Name the blood parasite species.
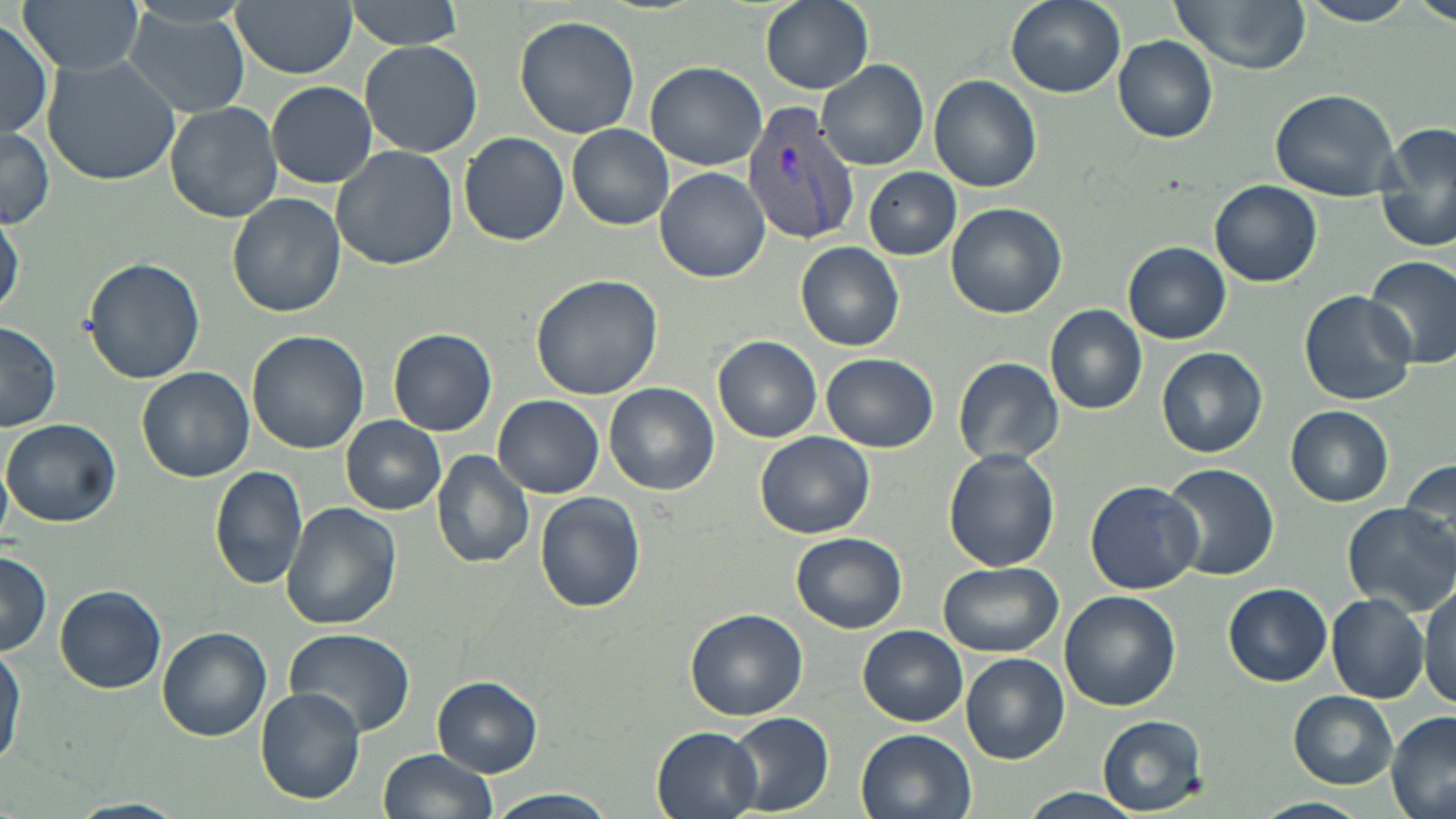

Plasmodium vivax.

Approximate bounding boxes as named x1/y1/x2/y2 corners in pixels. Uninfected red blood cell locations: (x1=16, y1=0, x2=145, y2=76), (x1=342, y1=0, x2=470, y2=49), (x1=760, y1=0, x2=874, y2=92), (x1=1004, y1=0, x2=1125, y2=98), (x1=1168, y1=0, x2=1312, y2=73), (x1=1300, y1=0, x2=1417, y2=26), (x1=1415, y1=0, x2=1456, y2=29), (x1=231, y1=1, x2=357, y2=77), (x1=122, y1=7, x2=254, y2=119), (x1=514, y1=15, x2=641, y2=139), (x1=0, y1=17, x2=55, y2=142), (x1=1113, y1=36, x2=1219, y2=143), (x1=360, y1=40, x2=483, y2=158), (x1=42, y1=55, x2=182, y2=186), (x1=815, y1=60, x2=929, y2=170), (x1=644, y1=61, x2=768, y2=171), (x1=930, y1=73, x2=1042, y2=192), (x1=266, y1=80, x2=377, y2=187), (x1=1271, y1=87, x2=1401, y2=200), (x1=165, y1=102, x2=283, y2=222), (x1=0, y1=125, x2=56, y2=228), (x1=568, y1=125, x2=675, y2=231), (x1=1377, y1=127, x2=1456, y2=255), (x1=459, y1=132, x2=569, y2=246), (x1=331, y1=144, x2=458, y2=269), (x1=655, y1=166, x2=770, y2=282), (x1=865, y1=168, x2=961, y2=261), (x1=1210, y1=180, x2=1322, y2=288), (x1=226, y1=192, x2=345, y2=317), (x1=946, y1=203, x2=1067, y2=318), (x1=0, y1=207, x2=24, y2=322), (x1=1123, y1=221, x2=1317, y2=337), (x1=1123, y1=241, x2=1231, y2=343), (x1=796, y1=242, x2=904, y2=351), (x1=1365, y1=253, x2=1456, y2=368), (x1=83, y1=257, x2=206, y2=385), (x1=531, y1=274, x2=662, y2=401), (x1=1297, y1=288, x2=1416, y2=405), (x1=1046, y1=305, x2=1148, y2=415), (x1=0, y1=321, x2=62, y2=431), (x1=389, y1=328, x2=498, y2=435), (x1=246, y1=330, x2=368, y2=453), (x1=714, y1=336, x2=823, y2=441), (x1=1156, y1=347, x2=1267, y2=457), (x1=821, y1=352, x2=938, y2=453), (x1=953, y1=356, x2=1064, y2=467), (x1=136, y1=366, x2=254, y2=482), (x1=604, y1=383, x2=720, y2=495), (x1=493, y1=397, x2=605, y2=498), (x1=1286, y1=405, x2=1394, y2=505), (x1=341, y1=417, x2=444, y2=514), (x1=3, y1=418, x2=121, y2=527), (x1=754, y1=432, x2=874, y2=538), (x1=943, y1=449, x2=1061, y2=572), (x1=431, y1=450, x2=535, y2=568), (x1=1400, y1=458, x2=1456, y2=557), (x1=0, y1=462, x2=12, y2=544), (x1=1161, y1=462, x2=1279, y2=580), (x1=209, y1=465, x2=310, y2=590), (x1=1085, y1=480, x2=1203, y2=594), (x1=534, y1=492, x2=646, y2=613), (x1=283, y1=503, x2=400, y2=627), (x1=1344, y1=503, x2=1455, y2=612), (x1=792, y1=533, x2=905, y2=632), (x1=0, y1=551, x2=52, y2=657), (x1=941, y1=562, x2=1063, y2=656), (x1=1419, y1=581, x2=1456, y2=707), (x1=1223, y1=583, x2=1333, y2=687), (x1=54, y1=585, x2=167, y2=694), (x1=1059, y1=592, x2=1180, y2=711), (x1=1326, y1=594, x2=1428, y2=702), (x1=686, y1=610, x2=807, y2=721), (x1=858, y1=624, x2=967, y2=726), (x1=157, y1=627, x2=272, y2=741), (x1=286, y1=629, x2=414, y2=737), (x1=0, y1=643, x2=23, y2=774), (x1=961, y1=654, x2=1069, y2=764), (x1=433, y1=675, x2=543, y2=778), (x1=255, y1=686, x2=367, y2=804), (x1=1288, y1=691, x2=1397, y2=789), (x1=728, y1=712, x2=834, y2=815), (x1=1387, y1=712, x2=1456, y2=819), (x1=1098, y1=715, x2=1207, y2=815), (x1=652, y1=727, x2=765, y2=819), (x1=855, y1=729, x2=978, y2=819), (x1=378, y1=750, x2=498, y2=819), (x1=1023, y1=788, x2=1140, y2=819), (x1=483, y1=789, x2=620, y2=819), (x1=1256, y1=797, x2=1367, y2=819), (x1=70, y1=798, x2=187, y2=819). Plasmodium vivax-infected red blood cell locations: (x1=741, y1=103, x2=864, y2=247). Captured at 1000x magnification. One field of a larger specimen. Image is 1456×819 pixels. Optical microscopy. May-Grünwald-Giemsa-stained preparation. Thin blood smear.